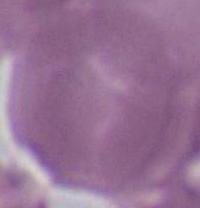

1000x magnification. An erythrocyte is seen. Photomicrograph.